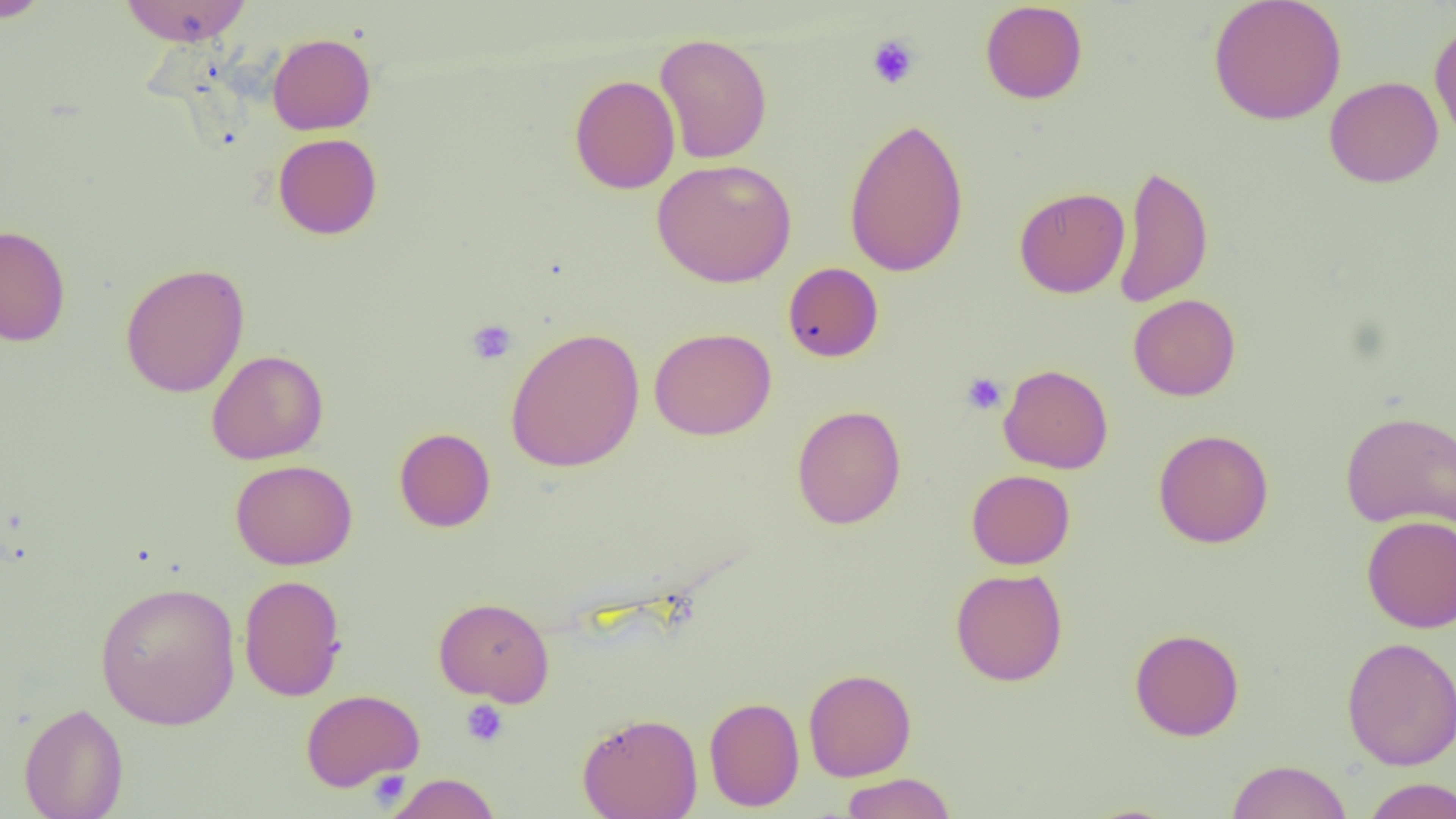
Approximate bounding boxes as named x1/y1/x2/y2 corners in pixels. Platelet locations: (x1=866, y1=34, x2=921, y2=90), (x1=466, y1=319, x2=517, y2=366), (x1=961, y1=372, x2=1007, y2=415), (x1=461, y1=699, x2=509, y2=747), (x1=368, y1=769, x2=413, y2=807). Uninfected red blood cell locations: (x1=1, y1=0, x2=52, y2=23), (x1=119, y1=0, x2=252, y2=45), (x1=1208, y1=0, x2=1347, y2=126), (x1=979, y1=1, x2=1088, y2=104), (x1=1428, y1=21, x2=1456, y2=145), (x1=267, y1=33, x2=376, y2=135), (x1=655, y1=33, x2=772, y2=164), (x1=569, y1=75, x2=681, y2=194), (x1=1324, y1=76, x2=1443, y2=188), (x1=843, y1=116, x2=969, y2=278), (x1=273, y1=133, x2=382, y2=239), (x1=652, y1=158, x2=797, y2=288), (x1=1113, y1=163, x2=1214, y2=308), (x1=1014, y1=186, x2=1129, y2=298), (x1=0, y1=224, x2=71, y2=346), (x1=783, y1=262, x2=883, y2=362), (x1=120, y1=263, x2=250, y2=398), (x1=1128, y1=294, x2=1241, y2=401), (x1=505, y1=327, x2=645, y2=473), (x1=649, y1=327, x2=776, y2=440), (x1=207, y1=350, x2=329, y2=464), (x1=998, y1=364, x2=1113, y2=474), (x1=791, y1=405, x2=906, y2=529), (x1=1340, y1=410, x2=1456, y2=531), (x1=394, y1=427, x2=496, y2=532), (x1=1153, y1=428, x2=1274, y2=548), (x1=230, y1=459, x2=358, y2=570), (x1=966, y1=469, x2=1075, y2=570), (x1=1361, y1=515, x2=1456, y2=632), (x1=950, y1=568, x2=1068, y2=686), (x1=239, y1=574, x2=347, y2=702), (x1=94, y1=581, x2=241, y2=731), (x1=433, y1=597, x2=555, y2=706), (x1=1129, y1=628, x2=1244, y2=741), (x1=1340, y1=636, x2=1456, y2=771), (x1=803, y1=668, x2=916, y2=781), (x1=300, y1=688, x2=425, y2=792), (x1=704, y1=696, x2=804, y2=811), (x1=19, y1=702, x2=129, y2=819), (x1=577, y1=712, x2=703, y2=819), (x1=1226, y1=759, x2=1352, y2=819), (x1=840, y1=772, x2=956, y2=819), (x1=384, y1=773, x2=502, y2=819), (x1=1361, y1=777, x2=1456, y2=819). Slide-level diagnosis: negative for blood parasites. 1000x magnification. Single field of view. Image is 1456×819 pixels. Optical microscopy. Thin blood smear.